Describe the morphology of the red blood cells.
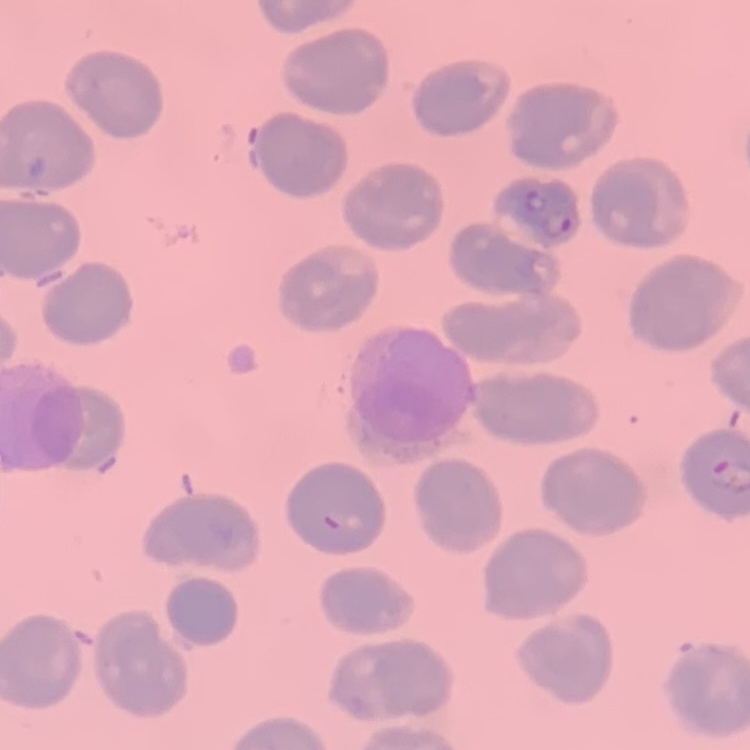

They show no rouleaux formation.

{
  "stain": "Field's or Giemsa",
  "image_type": "square crop of a larger photomicrograph",
  "preparation": "thin blood smear"
}